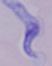

Summary:
  - Modality: micrograph
  - Identification: trypanosome
  - Magnification: 1000x